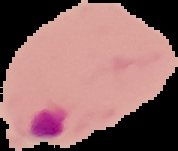
Summary:
  - Malaria status: parasitized
  - Image size: 178×151 pixels
  - Preparation: thin blood film
  - Image type: cell region segmented out of the field of view; surrounding area masked to black